Name the parasite shown.
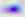

This is Toxoplasma gondii.

Micrograph. 400x magnification.